Outline each blood parasite and name the species.
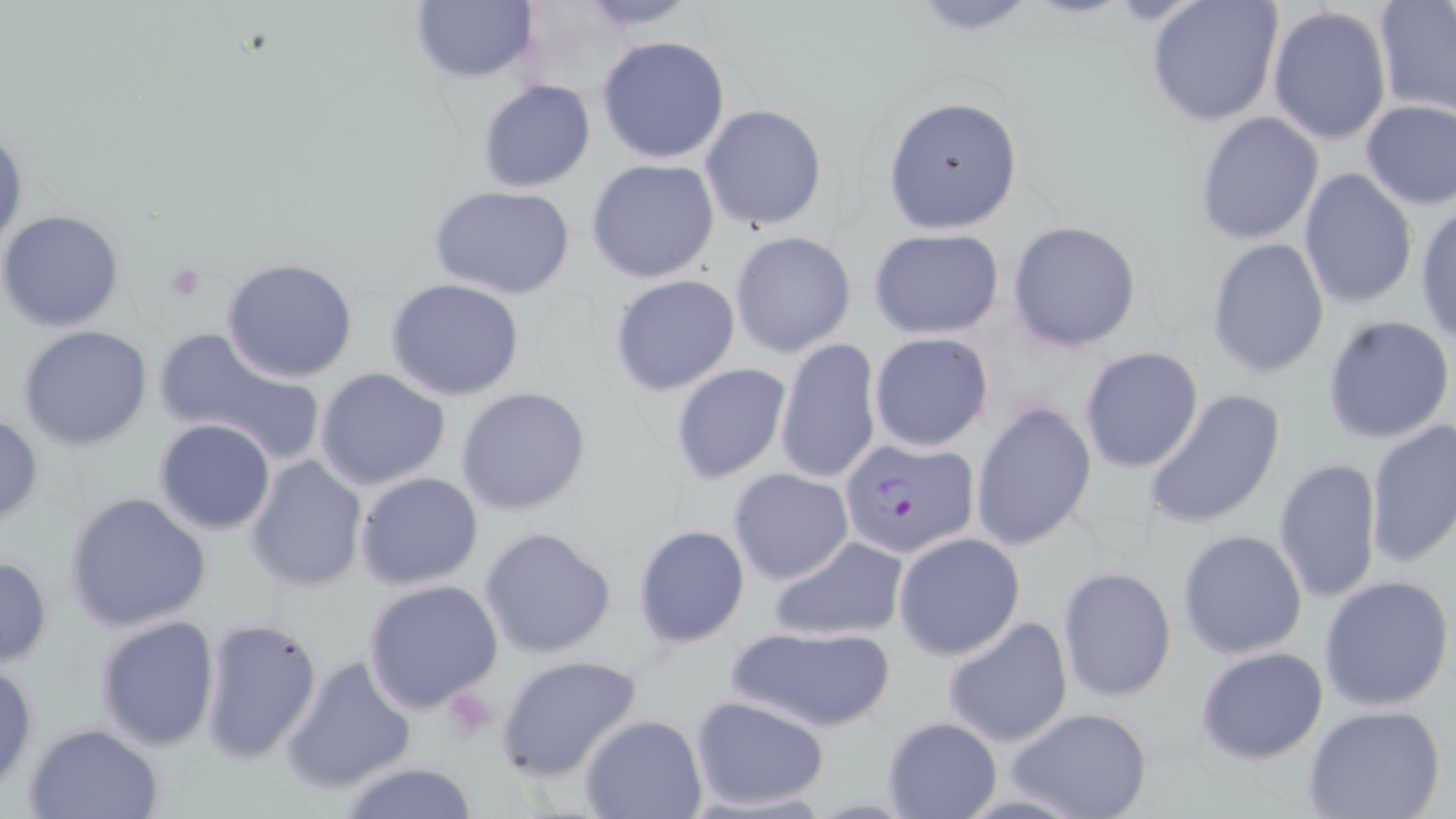

Approximate bounding boxes as (x1, y1, x2, y2) in pixels.
Plasmodium falciparum-infected red blood cells: (841, 437, 978, 560).
No Plasmodium ovale, Plasmodium malariae, Plasmodium vivax, Babesia divergens, or Trypanosoma brucei observed.

Platelet locations: (164, 264, 206, 303). Uninfected red blood cell locations: (408, 0, 539, 83), (570, 0, 706, 30), (900, 0, 1051, 34), (1147, 0, 1284, 128), (1374, 2, 1456, 118), (1268, 5, 1394, 146), (596, 35, 730, 163), (477, 80, 596, 192), (882, 95, 1024, 234), (1358, 100, 1456, 211), (700, 103, 828, 233), (1194, 111, 1324, 247), (0, 118, 26, 255), (586, 158, 720, 284), (1298, 169, 1418, 309), (429, 184, 577, 299), (1414, 202, 1456, 345), (1, 209, 126, 331), (1008, 220, 1140, 351), (867, 228, 1005, 340), (729, 231, 856, 358), (1205, 238, 1330, 378), (222, 258, 358, 384), (609, 275, 741, 396), (386, 277, 524, 400), (1322, 314, 1456, 445), (18, 326, 153, 449), (154, 327, 327, 464), (868, 332, 994, 452), (776, 338, 882, 485), (1079, 346, 1203, 472), (668, 362, 792, 486), (314, 367, 451, 492), (456, 386, 592, 516), (1142, 386, 1288, 531), (970, 399, 1095, 553), (0, 408, 43, 530), (152, 419, 275, 535), (1363, 421, 1456, 568), (246, 455, 369, 593), (1273, 457, 1382, 604), (728, 467, 855, 584), (355, 472, 484, 592), (62, 490, 212, 633), (631, 523, 750, 649), (477, 525, 617, 658), (1176, 529, 1308, 660), (892, 532, 1025, 660), (768, 534, 909, 644), (0, 555, 52, 667), (1059, 567, 1176, 702), (1318, 574, 1455, 713), (362, 578, 504, 714), (196, 614, 323, 764), (94, 615, 220, 750), (943, 616, 1073, 749), (722, 625, 900, 734), (1195, 646, 1330, 764), (279, 654, 418, 792), (495, 654, 642, 783), (0, 661, 38, 794), (688, 695, 830, 811), (1007, 707, 1153, 819), (1303, 707, 1446, 819), (578, 714, 707, 819), (880, 716, 1001, 819), (23, 722, 166, 819), (337, 762, 481, 818). Slide-level diagnosis: Plasmodium falciparum. Optical microscopy. May-Grünwald-Giemsa stain. Image is 1456×819 pixels. Single field of view. 1000x magnification. Thin blood film.